State which cell type is depicted.
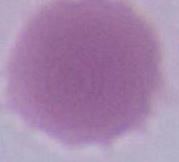

This is an erythrocyte.

Photomicrograph. Captured at 1000x magnification.